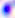
Summary:
  - Modality: photomicrograph
  - Magnification: 400x
  - Identification: Toxoplasma gondii